Outline each Plasmodium ovale-infected red blood cell.
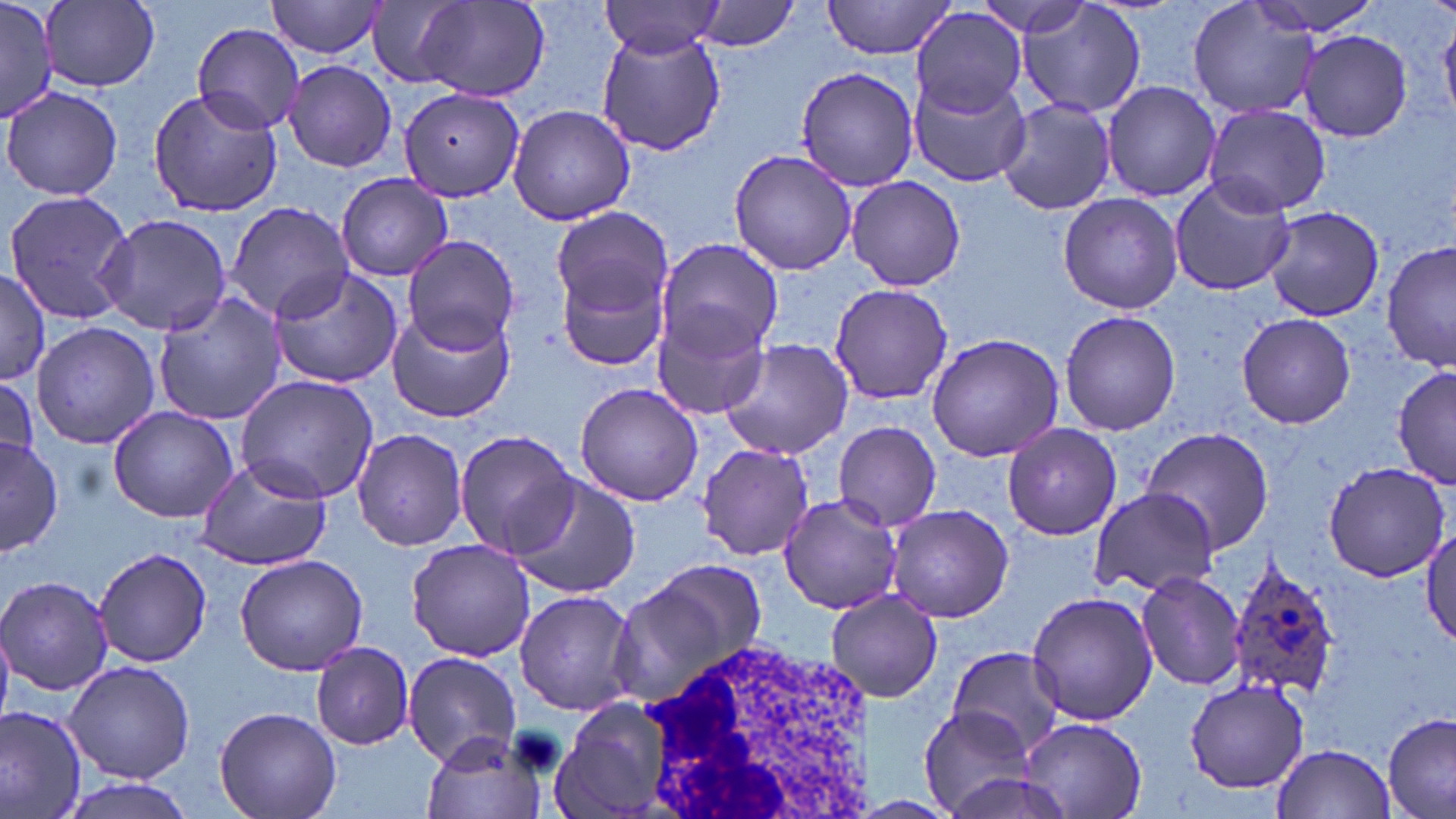
Approximate bounding boxes as [x1, y1, x2, y2] in pixels.
Plasmodium ovale-infected red blood cells: [1226, 556, 1343, 704].

Summary:
  - Uninfected red blood cell locations: [266, 0, 392, 60], [409, 0, 552, 103], [692, 0, 802, 53], [823, 0, 957, 58], [969, 0, 1100, 37], [1018, 0, 1144, 119], [1245, 0, 1389, 36], [41, 1, 160, 91], [365, 1, 474, 89], [1188, 1, 1319, 120], [0, 2, 56, 123], [599, 2, 726, 58], [912, 8, 1028, 116], [193, 23, 306, 134], [1296, 28, 1413, 143], [597, 32, 726, 157], [283, 60, 398, 172], [792, 65, 921, 192], [910, 72, 1034, 185], [1100, 80, 1220, 203], [3, 86, 123, 202], [397, 86, 525, 203], [146, 88, 284, 217], [994, 97, 1117, 215], [1203, 103, 1331, 218], [507, 104, 636, 226], [728, 148, 856, 277], [334, 172, 452, 281], [845, 174, 966, 292], [1168, 177, 1295, 298], [1, 190, 136, 324], [1056, 192, 1183, 314], [222, 201, 352, 321], [552, 206, 673, 317], [1264, 208, 1385, 320], [97, 212, 232, 336], [402, 233, 520, 352], [657, 240, 781, 357], [1381, 242, 1454, 372], [555, 251, 673, 375], [267, 264, 405, 388], [0, 271, 54, 390], [828, 282, 954, 406], [151, 291, 291, 427], [386, 305, 516, 425], [649, 306, 773, 422], [1058, 310, 1181, 436], [1235, 313, 1356, 427], [33, 320, 159, 450], [924, 332, 1063, 463], [717, 339, 853, 460], [1393, 360, 1455, 489], [0, 373, 43, 479], [235, 375, 380, 503], [573, 382, 703, 507], [106, 405, 241, 524], [832, 421, 943, 530], [1000, 423, 1123, 540], [1137, 426, 1276, 553], [354, 429, 469, 551], [454, 429, 581, 559], [0, 435, 64, 559], [698, 443, 812, 561], [191, 455, 333, 571], [1323, 461, 1450, 582], [507, 473, 640, 601], [1091, 485, 1217, 598], [778, 493, 905, 615], [886, 504, 1015, 623], [1422, 526, 1456, 652], [406, 537, 535, 662], [93, 546, 214, 667], [233, 554, 370, 676], [614, 562, 765, 709], [1137, 570, 1246, 692], [0, 576, 117, 697], [824, 588, 943, 704], [514, 589, 636, 714], [1025, 591, 1158, 727], [309, 641, 415, 749], [946, 648, 1064, 754], [403, 651, 522, 768], [65, 659, 194, 785], [1184, 681, 1309, 792], [549, 697, 674, 818], [0, 704, 86, 819], [916, 705, 1040, 818], [212, 707, 343, 819], [1381, 712, 1456, 819], [1018, 718, 1146, 817], [422, 729, 546, 819], [1271, 743, 1397, 819]
  - White blood cell locations: [636, 636, 876, 819]
  - Slide-level diagnosis: Plasmodium ovale
  - Modality: optical microscopy
  - Magnification: 1000x
  - Field of view: single
  - Stain: May-Grünwald-Giemsa
  - Image size: 1456×819 pixels
  - Preparation: thin blood film